Name the parasite shown.
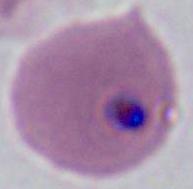
This is Plasmodium.

Photomicrograph. 400x or 1000x magnification.